Locate every Plasmodium malariae-infected red blood cell.
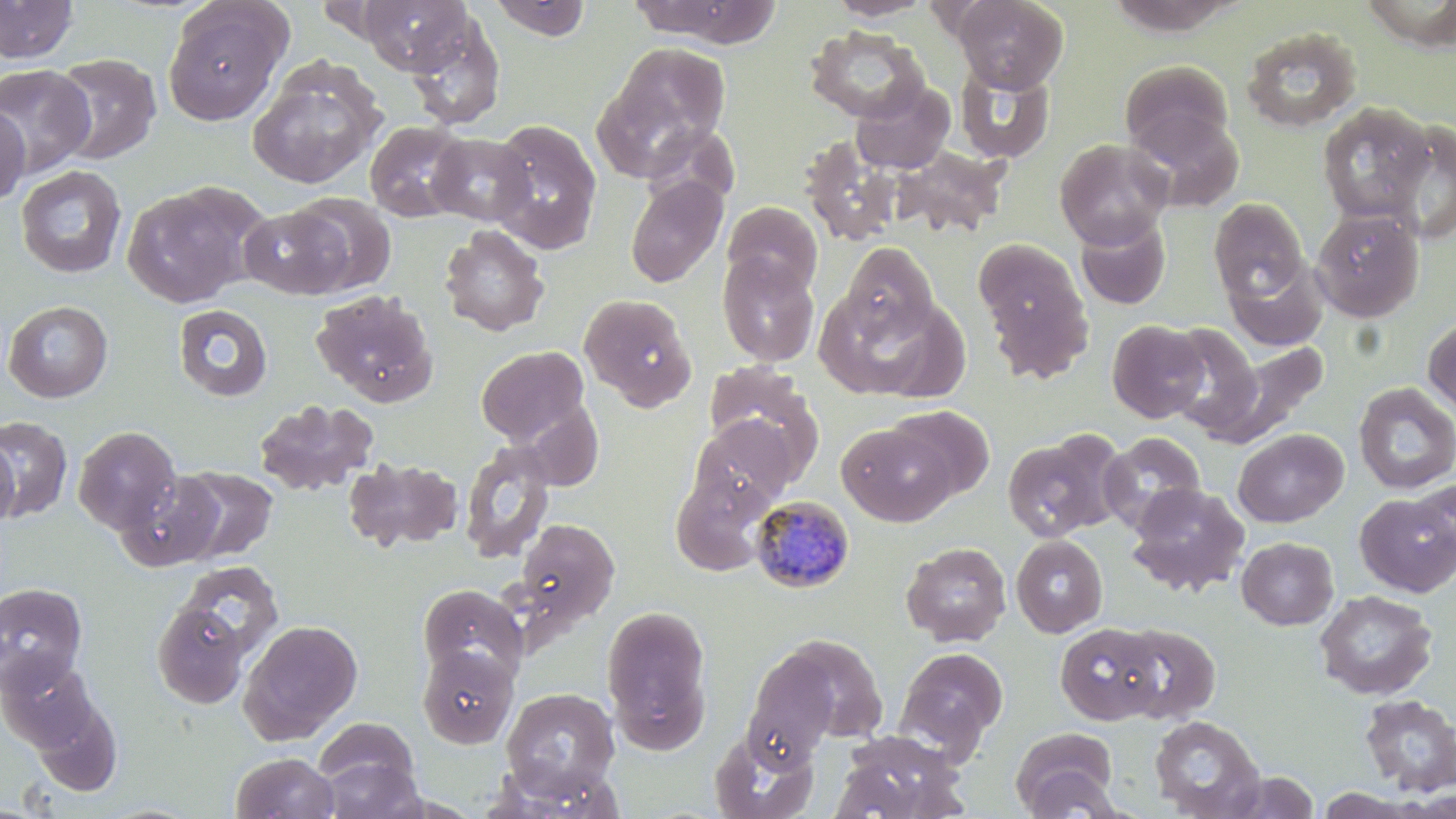
Approximate bounding boxes as named x1/y1/x2/y2 corners in pixels.
Plasmodium malariae-infected red blood cells: (x1=751, y1=496, x2=855, y2=593).

{
  "slide_level_diagnosis": "Plasmodium malariae",
  "field_of_view": "single",
  "magnification": "1000x",
  "image_size": "1456×819 pixels",
  "modality": "optical microscopy",
  "preparation": "thin blood film",
  "stain": "May-Grünwald-Giemsa",
  "uninfected_red_blood_cell_locations": "approximate bounding boxes as named x1/y1/x2/y2 corners in pixels: (x1=0, y1=0, x2=79, y2=63), (x1=358, y1=0, x2=472, y2=74), (x1=629, y1=0, x2=782, y2=47), (x1=825, y1=0, x2=935, y2=20), (x1=953, y1=0, x2=1068, y2=92), (x1=487, y1=1, x2=595, y2=41), (x1=1361, y1=1, x2=1456, y2=47), (x1=162, y1=2, x2=289, y2=126), (x1=406, y1=16, x2=506, y2=130), (x1=804, y1=25, x2=929, y2=123), (x1=1240, y1=26, x2=1362, y2=133), (x1=596, y1=43, x2=732, y2=176), (x1=50, y1=53, x2=162, y2=164), (x1=248, y1=58, x2=385, y2=189), (x1=1119, y1=60, x2=1235, y2=157), (x1=955, y1=63, x2=1055, y2=163), (x1=0, y1=64, x2=95, y2=178), (x1=851, y1=80, x2=955, y2=175), (x1=0, y1=102, x2=29, y2=207), (x1=1317, y1=103, x2=1434, y2=223), (x1=1127, y1=108, x2=1244, y2=213), (x1=487, y1=119, x2=603, y2=255), (x1=364, y1=120, x2=469, y2=222), (x1=1383, y1=120, x2=1456, y2=245), (x1=427, y1=132, x2=536, y2=226), (x1=800, y1=136, x2=902, y2=246), (x1=1054, y1=138, x2=1174, y2=248), (x1=893, y1=146, x2=1009, y2=239), (x1=15, y1=165, x2=127, y2=279), (x1=625, y1=174, x2=728, y2=288), (x1=121, y1=181, x2=266, y2=308), (x1=287, y1=193, x2=396, y2=294), (x1=1208, y1=198, x2=1309, y2=304), (x1=723, y1=201, x2=823, y2=296), (x1=239, y1=204, x2=352, y2=299), (x1=1311, y1=206, x2=1424, y2=322), (x1=1074, y1=213, x2=1172, y2=311), (x1=439, y1=224, x2=549, y2=337), (x1=974, y1=238, x2=1094, y2=378), (x1=841, y1=242, x2=938, y2=342), (x1=717, y1=252, x2=820, y2=367), (x1=1225, y1=258, x2=1328, y2=352), (x1=311, y1=289, x2=439, y2=407), (x1=817, y1=289, x2=954, y2=399), (x1=580, y1=293, x2=697, y2=411), (x1=3, y1=300, x2=113, y2=403), (x1=172, y1=304, x2=273, y2=402), (x1=1422, y1=316, x2=1456, y2=418), (x1=1106, y1=320, x2=1209, y2=422), (x1=1163, y1=322, x2=1266, y2=439), (x1=1210, y1=338, x2=1330, y2=446), (x1=476, y1=345, x2=589, y2=444), (x1=702, y1=363, x2=823, y2=481), (x1=1353, y1=383, x2=1456, y2=494), (x1=253, y1=399, x2=378, y2=497), (x1=517, y1=403, x2=604, y2=492), (x1=888, y1=405, x2=995, y2=501), (x1=689, y1=415, x2=800, y2=514), (x1=1, y1=416, x2=73, y2=521), (x1=837, y1=422, x2=955, y2=525), (x1=73, y1=426, x2=181, y2=534), (x1=1232, y1=428, x2=1348, y2=528), (x1=1099, y1=431, x2=1206, y2=532), (x1=1001, y1=433, x2=1118, y2=542), (x1=0, y1=438, x2=20, y2=526), (x1=459, y1=441, x2=557, y2=564), (x1=343, y1=457, x2=463, y2=553), (x1=175, y1=465, x2=278, y2=562), (x1=671, y1=468, x2=774, y2=574), (x1=118, y1=470, x2=226, y2=571), (x1=1412, y1=480, x2=1456, y2=569), (x1=1127, y1=483, x2=1249, y2=597), (x1=1355, y1=492, x2=1456, y2=597), (x1=515, y1=519, x2=619, y2=625), (x1=1011, y1=535, x2=1108, y2=637), (x1=1236, y1=537, x2=1339, y2=629), (x1=901, y1=541, x2=1012, y2=646), (x1=176, y1=561, x2=284, y2=662), (x1=0, y1=583, x2=88, y2=692), (x1=417, y1=583, x2=527, y2=686), (x1=1314, y1=590, x2=1437, y2=700), (x1=152, y1=600, x2=252, y2=708), (x1=601, y1=603, x2=714, y2=750), (x1=239, y1=620, x2=363, y2=744), (x1=1055, y1=622, x2=1166, y2=727), (x1=1115, y1=624, x2=1220, y2=724), (x1=758, y1=633, x2=890, y2=750), (x1=416, y1=645, x2=518, y2=749), (x1=895, y1=647, x2=1009, y2=755), (x1=1, y1=657, x2=99, y2=751), (x1=501, y1=687, x2=620, y2=796), (x1=28, y1=693, x2=123, y2=795), (x1=1358, y1=694, x2=1456, y2=794), (x1=1149, y1=715, x2=1265, y2=818), (x1=312, y1=716, x2=421, y2=804), (x1=1011, y1=727, x2=1121, y2=818), (x1=710, y1=728, x2=818, y2=818), (x1=832, y1=730, x2=968, y2=819), (x1=231, y1=752, x2=340, y2=818), (x1=1221, y1=771, x2=1321, y2=818), (x1=1315, y1=788, x2=1434, y2=818)"
}